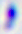
Summary:
  - Identification: Toxoplasma gondii
  - Magnification: 400x
  - Modality: micrograph